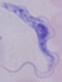
magnification = 1000x
identification = trypanosome
modality = photomicrograph